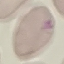

Summary:
  - Malaria status: uninfected
  - Stain: Giemsa
  - Image type: automatically extracted cell patch, resized to 64 × 64 pixels
  - Capture: smartphone camera at the microscope eyepiece
  - Preparation: thin smear